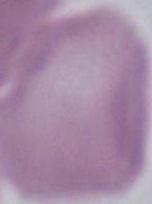
identification = erythrocyte
modality = photomicrograph
magnification = 1000x